Identify the parasite.
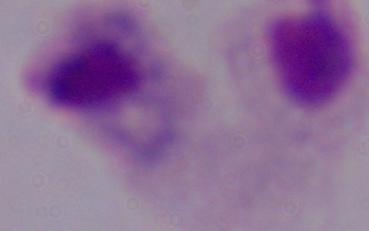
A trichomonad.

Photomicrograph. Captured at 1000x magnification.